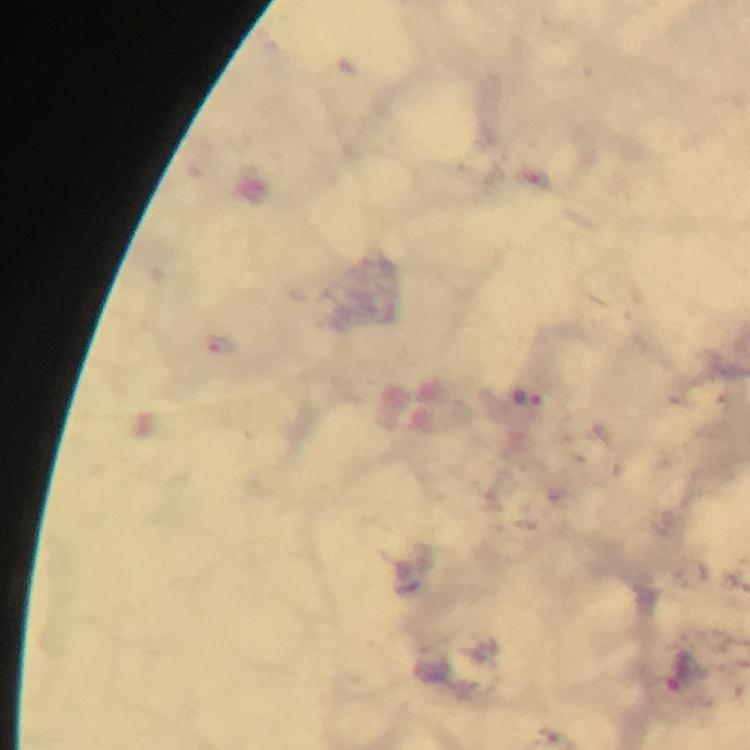
Approximate centers as (x, y) in pixels.
Summary:
  - Plasmodium parasite locations: (220, 347)
  - Stain: Giemsa
  - Immersion oil: used
  - Preparation: thick blood smear
  - Context: from a malaria diagnostic workup
  - Image size: 750×750 pixels
  - Capture: smartphone camera through the microscope
  - Magnification: 100x
  - Cropped from: one field of view